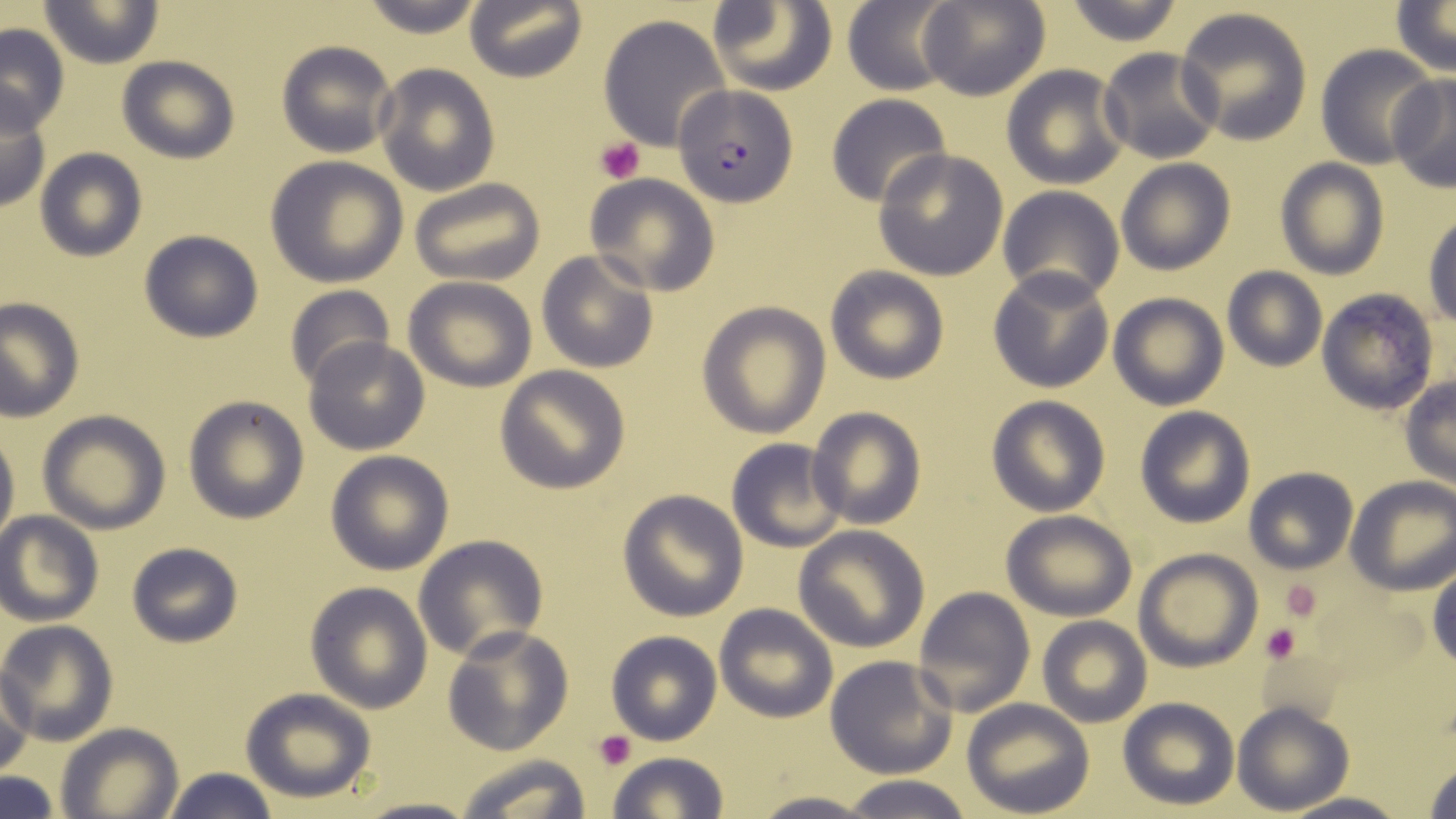
Summary:
  - Coordinate format: approximate bounding boxes as (x1, y1, x2, y2) in pixels
  - Platelet locations: (596, 138, 645, 184), (1280, 580, 1325, 623), (1261, 622, 1301, 665), (592, 731, 638, 769)
  - Uninfected red blood cell locations: (41, 0, 162, 68), (356, 0, 488, 38), (706, 0, 837, 95), (843, 0, 962, 95), (918, 0, 1049, 102), (1060, 0, 1185, 46), (465, 1, 587, 83), (1391, 1, 1455, 74), (1172, 5, 1315, 144), (598, 13, 734, 152), (0, 23, 70, 134), (276, 39, 397, 157), (1315, 44, 1441, 167), (1097, 47, 1222, 164), (117, 55, 239, 165), (374, 63, 500, 195), (1001, 64, 1128, 190), (1385, 72, 1456, 193), (0, 94, 51, 214), (825, 94, 952, 207), (34, 148, 148, 261), (872, 148, 1009, 280), (264, 155, 410, 286), (1275, 157, 1390, 279), (1116, 158, 1235, 275), (584, 175, 720, 295), (411, 177, 546, 287), (997, 185, 1126, 305), (1424, 209, 1456, 328), (140, 230, 265, 343), (537, 249, 658, 372), (826, 266, 948, 384), (987, 266, 1115, 392), (1222, 267, 1326, 371), (401, 276, 537, 392), (283, 285, 394, 390), (1315, 290, 1440, 414), (1108, 292, 1229, 410), (0, 298, 83, 420), (697, 302, 831, 438), (304, 336, 429, 455), (496, 366, 631, 494), (1400, 377, 1456, 490), (986, 395, 1112, 517), (182, 396, 309, 522), (808, 406, 926, 529), (1135, 406, 1256, 528), (37, 410, 171, 534), (0, 423, 18, 553), (725, 438, 848, 552), (324, 451, 454, 575), (1244, 468, 1359, 574), (1346, 475, 1456, 595), (616, 489, 749, 622), (1002, 510, 1137, 621), (0, 512, 103, 625), (794, 524, 929, 652), (413, 535, 548, 663), (125, 541, 244, 650), (1134, 549, 1262, 672), (1429, 566, 1455, 671), (303, 580, 433, 713), (913, 586, 1034, 717), (714, 602, 837, 723), (1038, 616, 1152, 728), (0, 620, 118, 747), (442, 625, 574, 756), (607, 631, 721, 744), (825, 655, 959, 779), (1, 667, 35, 778), (239, 688, 376, 803), (1116, 697, 1239, 809), (961, 700, 1095, 819), (1232, 702, 1352, 814), (56, 723, 184, 819), (605, 751, 730, 819), (450, 754, 594, 819), (1420, 757, 1456, 818), (163, 767, 279, 819), (0, 773, 61, 819), (839, 775, 976, 819), (745, 791, 880, 819), (1282, 791, 1409, 819), (350, 796, 483, 819)
  - Plasmodium falciparum-infected red blood cell locations: (674, 84, 796, 207)
  - Slide-level diagnosis: Plasmodium falciparum
  - Stain: May-Grünwald-Giemsa
  - Image size: 1456×819 pixels
  - Modality: optical microscopy
  - Preparation: thin blood film
  - Magnification: 1000x
  - Field of view: one of a larger specimen